Classify this cell by malaria status.
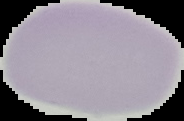

It is uninfected.

Summary:
  - Preparation: thin blood smear
  - Image size: 184×121 pixels
  - Image type: segmented cell region on a black background